Assess this cell for malaria.
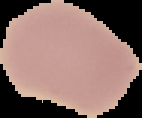

Uninfected.

Image is 142×118 pixels. The area outside the segmented cell region is set to black. From a thin blood smear.